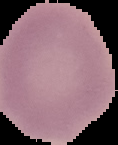 Malaria status: uninfected. Image is 118×145 pixels. The area outside the segmented cell region is set to black. From a thin blood film.